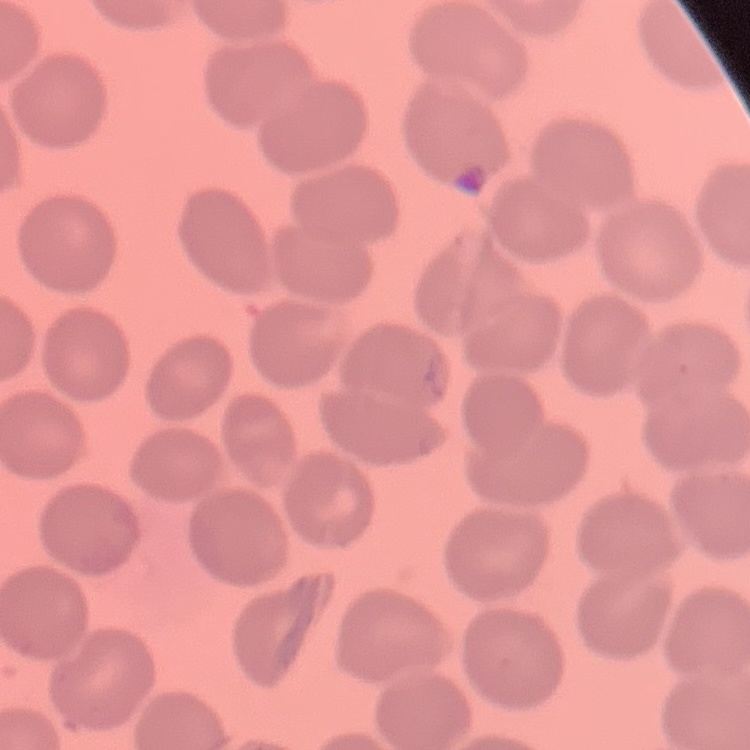

Summary:
  - Red blood cell morphology: no rouleaux formation
  - Preparation: thin peripheral smear
  - Image type: one tile cut from a larger photomicrograph
  - Stain: Field's or Giemsa